Name the blood parasite species.
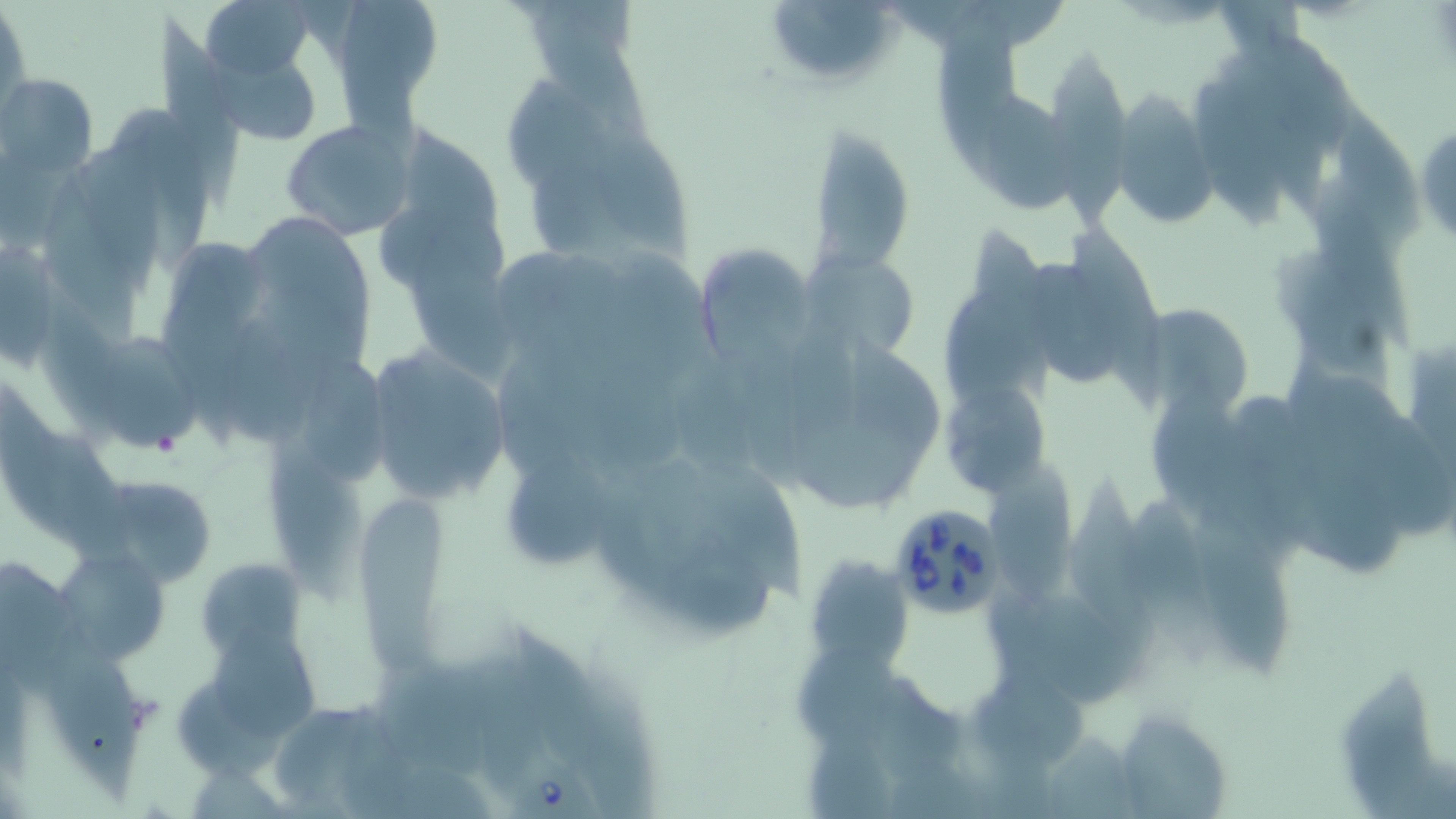

Babesia divergens.

Approximate bounding boxes as (x1,y1)-(x2,y2) corner pairs in pixels. Babesia divergens-infected red blood cell locations: (887,501)-(1009,618), (507,750)-(601,819). Uninfected red blood cell locations: (202,0)-(314,82), (764,0)-(903,92), (1,8)-(30,124), (522,10)-(651,139), (935,15)-(1027,175), (3,73)-(98,180), (1109,92)-(1221,229), (981,93)-(1079,215), (1333,97)-(1421,247), (117,103)-(213,278), (594,116)-(689,261), (1412,118)-(1456,246), (279,119)-(413,238), (809,122)-(915,273), (414,229)-(513,384), (701,249)-(820,363), (809,249)-(920,364), (1028,255)-(1122,390), (1137,305)-(1254,419), (102,333)-(205,454), (364,347)-(513,504), (301,360)-(396,490), (942,374)-(1051,496), (265,437)-(360,599), (508,454)-(619,567), (987,466)-(1082,605), (86,473)-(224,585), (1062,473)-(1160,647), (358,496)-(452,672), (1131,496)-(1216,664), (1188,502)-(1290,679), (54,554)-(172,664), (813,556)-(920,675), (201,564)-(311,662), (46,631)-(147,803), (220,638)-(324,738), (794,644)-(903,749), (377,661)-(505,786), (1110,708)-(1235,819). Light microscopy. May-Grünwald-Giemsa stain. Image is 1456×819 pixels. One field of a larger specimen. 1000x magnification. Thin blood film.